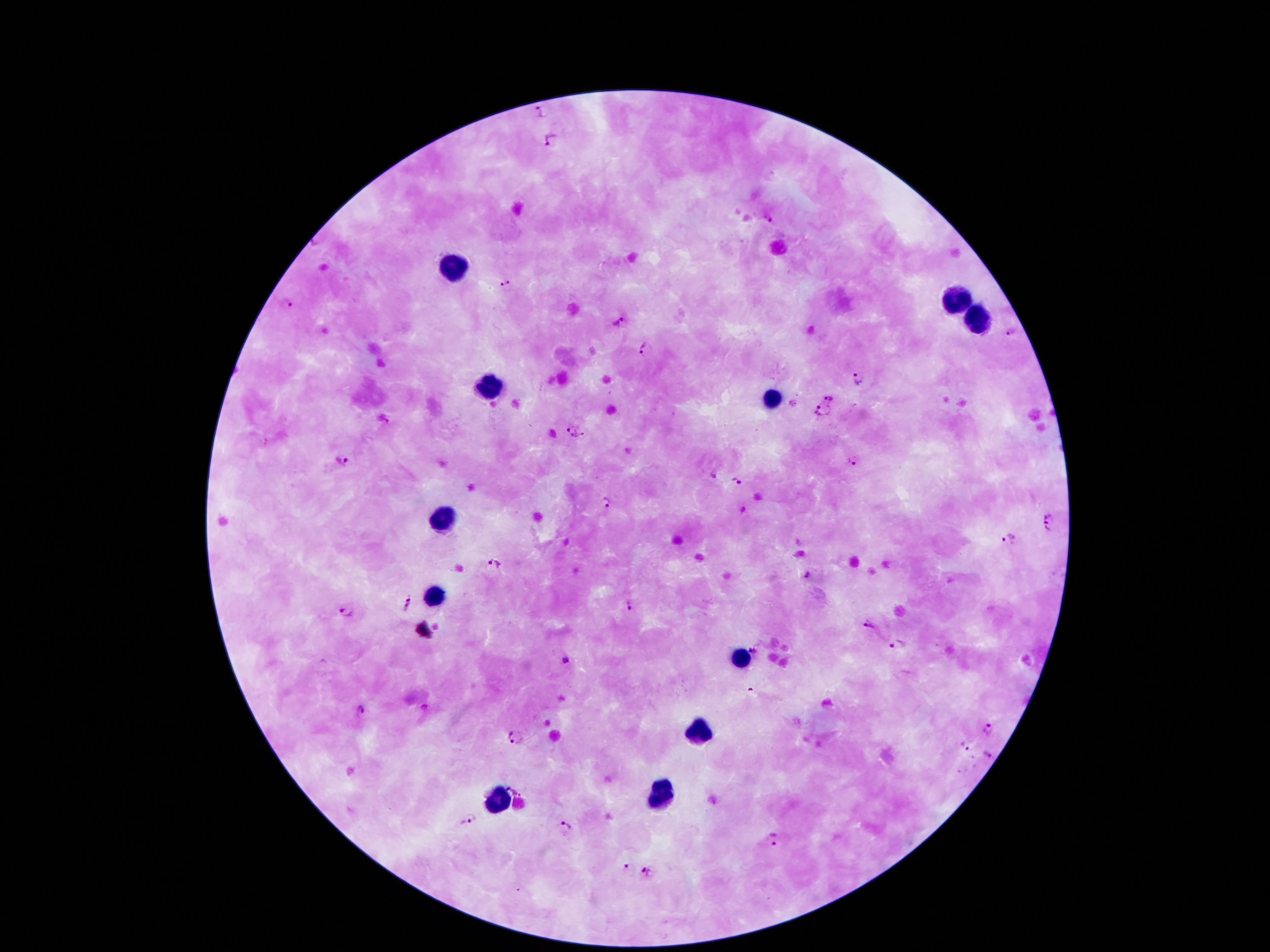
Approximate centers as [x, y] in pixels. Leukocyte locations: [452, 261], [956, 302], [974, 320], [489, 388], [771, 398], [443, 519], [435, 593], [741, 658], [698, 736], [663, 796], [499, 802]. Plasmodium parasite locations: [542, 110], [549, 137], [768, 219], [507, 282], [285, 303], [618, 322], [1009, 330], [643, 348], [859, 378], [829, 395], [821, 413], [572, 432], [341, 462], [855, 462], [713, 476], [737, 478], [606, 501], [1051, 522], [1012, 539], [494, 564], [809, 575], [408, 606], [629, 606], [346, 612], [872, 625], [899, 647], [566, 661], [361, 710], [989, 730], [515, 736], [963, 748], [988, 756], [513, 787], [470, 820], [564, 828], [773, 838], [627, 868], [649, 873]. Patient malaria status: infected with Plasmodium falciparum. 100x magnification. Giemsa-stained preparation. Thick blood film. One field from this slide. Photographed through the microscope eyepiece with a smartphone camera. Image is 1270×952 pixels.